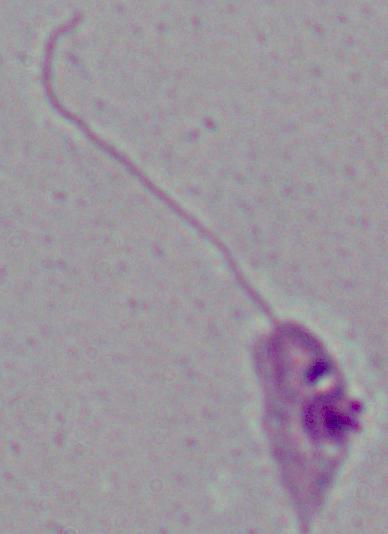
A Leishmania parasite is shown. Micrograph. Captured at 1000x magnification.